Classify this cell by malaria status.
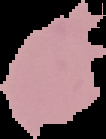
Uninfected.

Summary:
  - Image type: cell region segmented out of the field of view; surrounding area masked to black
  - Image size: 106×139 pixels
  - Preparation: thin blood smear